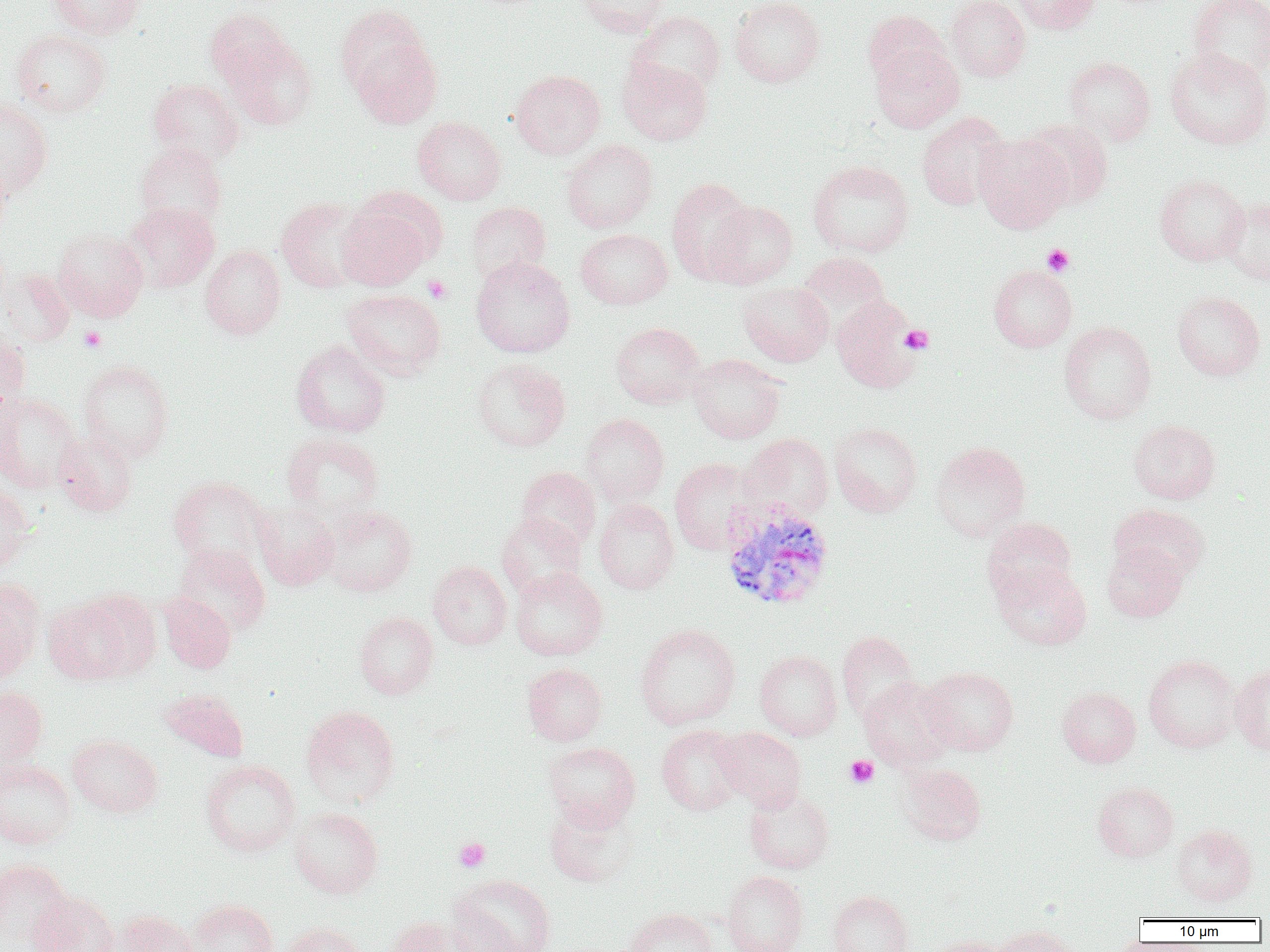
{
  "slide_level_diagnosis": "Plasmodium vivax",
  "field_of_view": "one of a larger specimen",
  "preparation": "thin blood film",
  "uninfected_red_blood_cell_locations": "approximate bounding boxes as (x1, y1, x2, y2) in pixels: (49, 0, 145, 39), (577, 0, 672, 38), (729, 0, 825, 88), (946, 0, 1030, 81), (1011, 0, 1101, 34), (1187, 0, 1270, 81), (335, 4, 429, 96), (205, 9, 292, 89), (629, 10, 725, 97), (863, 10, 949, 87), (11, 29, 111, 118), (351, 36, 442, 129), (225, 37, 318, 131), (870, 43, 964, 133), (1164, 48, 1270, 150), (617, 56, 712, 146), (1063, 56, 1156, 146), (510, 69, 606, 160), (148, 79, 245, 166), (0, 98, 52, 198), (916, 111, 1012, 211), (412, 117, 507, 205), (1020, 119, 1114, 210), (973, 133, 1072, 233), (562, 139, 658, 233), (135, 142, 227, 231), (0, 155, 12, 239), (808, 160, 914, 257), (1154, 174, 1249, 266), (666, 177, 755, 284), (275, 196, 374, 292), (1219, 197, 1270, 285), (337, 199, 437, 291), (466, 201, 550, 283), (705, 201, 797, 289), (125, 202, 219, 292), (53, 228, 149, 321), (575, 229, 673, 310), (200, 245, 286, 339), (797, 251, 890, 335), (471, 256, 574, 358), (988, 264, 1077, 352), (0, 268, 74, 346), (738, 282, 833, 367), (341, 289, 446, 380), (1171, 291, 1266, 381), (832, 296, 922, 393), (1059, 321, 1157, 424), (610, 322, 706, 409), (0, 326, 30, 417), (291, 340, 390, 438), (688, 354, 787, 444), (471, 357, 571, 452), (78, 359, 175, 462), (0, 392, 81, 492), (581, 413, 669, 506), (1128, 420, 1221, 504), (829, 422, 922, 517), (53, 431, 138, 518), (281, 432, 385, 519), (739, 433, 834, 522), (930, 441, 1031, 541), (669, 458, 763, 555), (516, 466, 601, 551), (169, 476, 270, 570), (0, 483, 33, 574), (594, 499, 679, 594), (253, 502, 339, 591), (1111, 503, 1210, 584), (321, 504, 417, 597), (496, 513, 586, 599), (981, 516, 1076, 603), (1101, 543, 1187, 622), (173, 544, 271, 638), (427, 562, 512, 650), (992, 562, 1092, 650), (510, 567, 608, 661), (0, 580, 44, 682), (158, 592, 236, 673), (43, 595, 138, 684), (354, 611, 438, 699), (634, 623, 741, 730), (836, 630, 920, 722), (754, 650, 842, 740), (1143, 654, 1241, 752), (522, 663, 607, 746), (1230, 663, 1270, 755), (920, 666, 1018, 755), (858, 677, 956, 770), (0, 686, 48, 774), (1057, 687, 1140, 767), (160, 689, 249, 762), (301, 705, 400, 808), (656, 725, 747, 815), (715, 727, 806, 811), (67, 734, 163, 818), (542, 742, 641, 830), (0, 758, 77, 849), (200, 759, 300, 857), (898, 763, 986, 845), (1092, 781, 1178, 862), (744, 786, 834, 875), (544, 798, 638, 888), (288, 807, 383, 899), (1172, 824, 1258, 906), (0, 858, 73, 952), (722, 871, 808, 952), (449, 874, 556, 952), (828, 890, 914, 952), (28, 892, 120, 952), (187, 899, 278, 952), (624, 908, 718, 952), (110, 909, 200, 952), (383, 916, 482, 952), (281, 922, 366, 952), (991, 925, 1082, 952), (924, 936, 1012, 952)",
  "image_size": "1270×952 pixels",
  "platelet_locations": "approximate bounding boxes as (x1, y1, x2, y2) in pixels: (1042, 244, 1075, 276), (422, 275, 452, 303), (79, 325, 106, 352), (900, 325, 933, 355), (845, 755, 879, 788), (454, 837, 490, 872)",
  "magnification": "1000x",
  "modality": "light microscopy",
  "plasmodium_vivax_infected_red_blood_cell_locations": "approximate bounding boxes as (x1, y1, x2, y2) in pixels: (718, 498, 835, 612)"
}